Describe the morphology of the red blood cells.
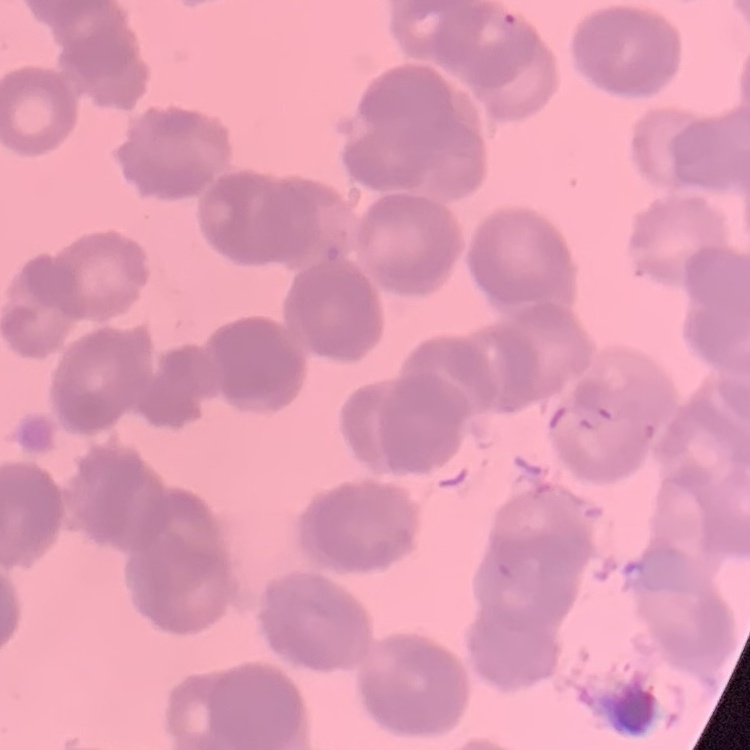

They show rouleaux formation.

preparation = thin blood smear
image type = square crop of a larger photomicrograph
stain = Field's or Giemsa